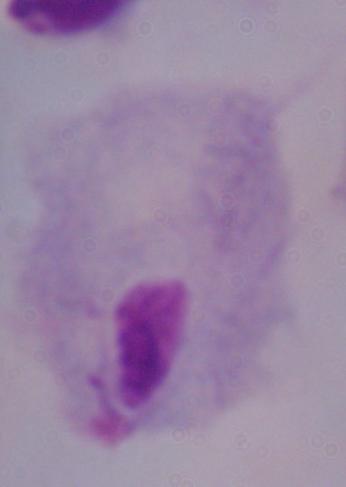
Micrograph. A trichomonad is shown. 1000x magnification.